Describe the morphology of the red blood cells.
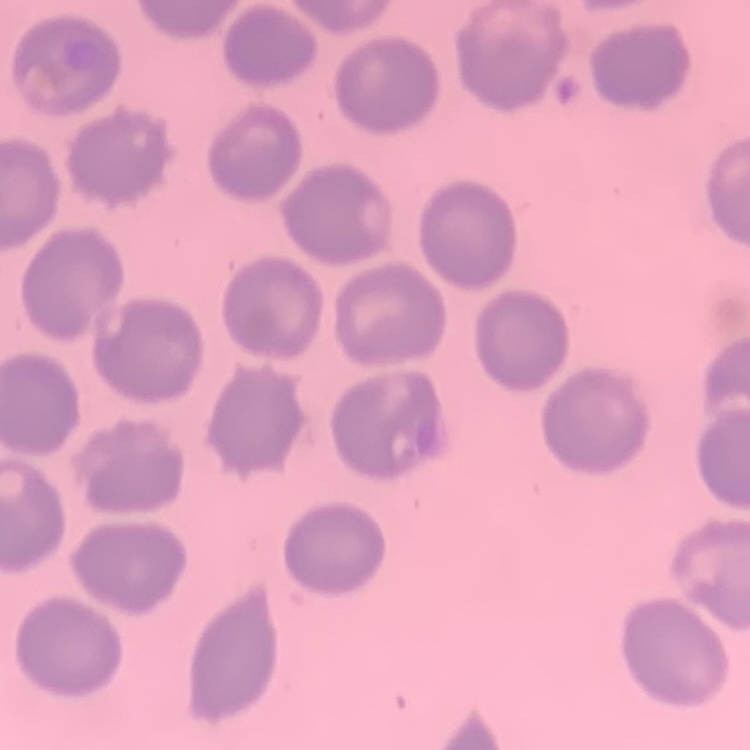
No rouleaux formation.

Field's or Giemsa stain. Square crop of a larger photomicrograph. Thin peripheral smear.